Classify this cell by malaria status.
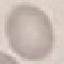

Uninfected.

{
  "image_type": "cell patch, automatically extracted from a larger field of view and resized to 64 × 64 pixels",
  "stain": "Giemsa",
  "preparation": "thin smear",
  "capture": "smartphone camera at the microscope eyepiece"
}